Name the parasite shown.
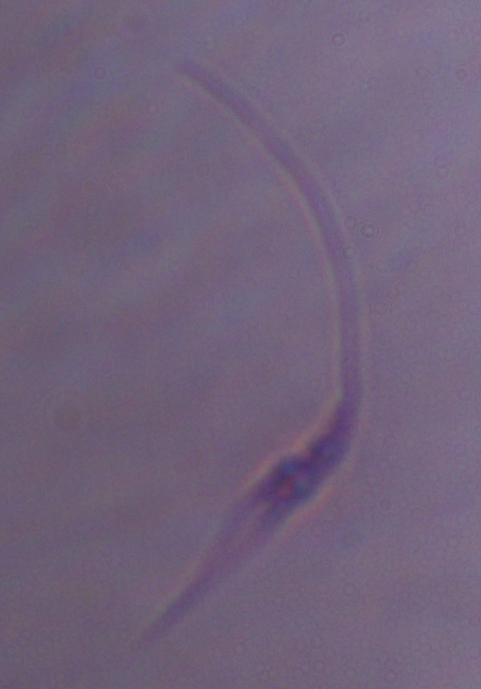

This is Leishmania.

magnification = 1000x
modality = micrograph